Assess the morphology of the erythrocytes.
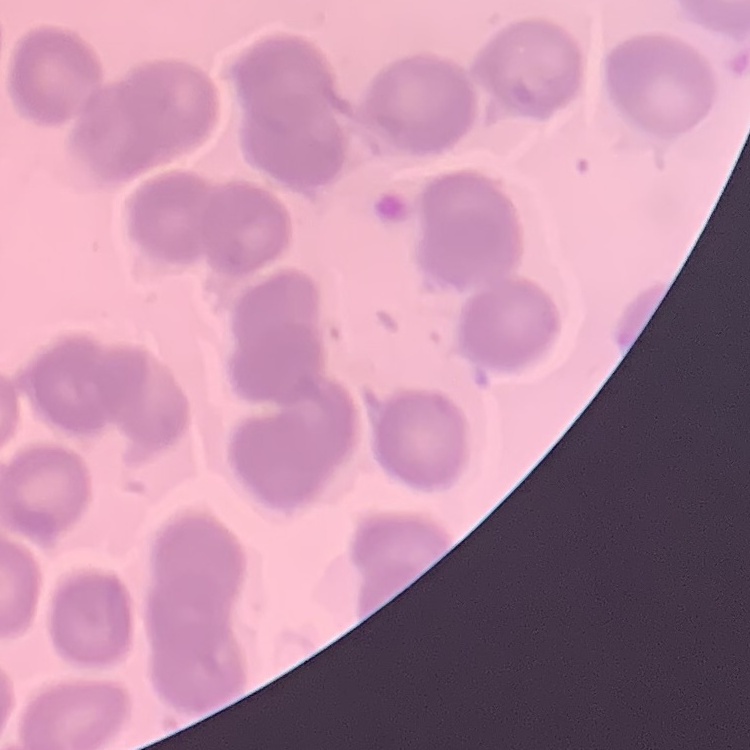

They show no rouleaux formation.

Field's or Giemsa stain. Square crop of a larger photomicrograph. Thin blood film.